Locate and identify every blood parasite.
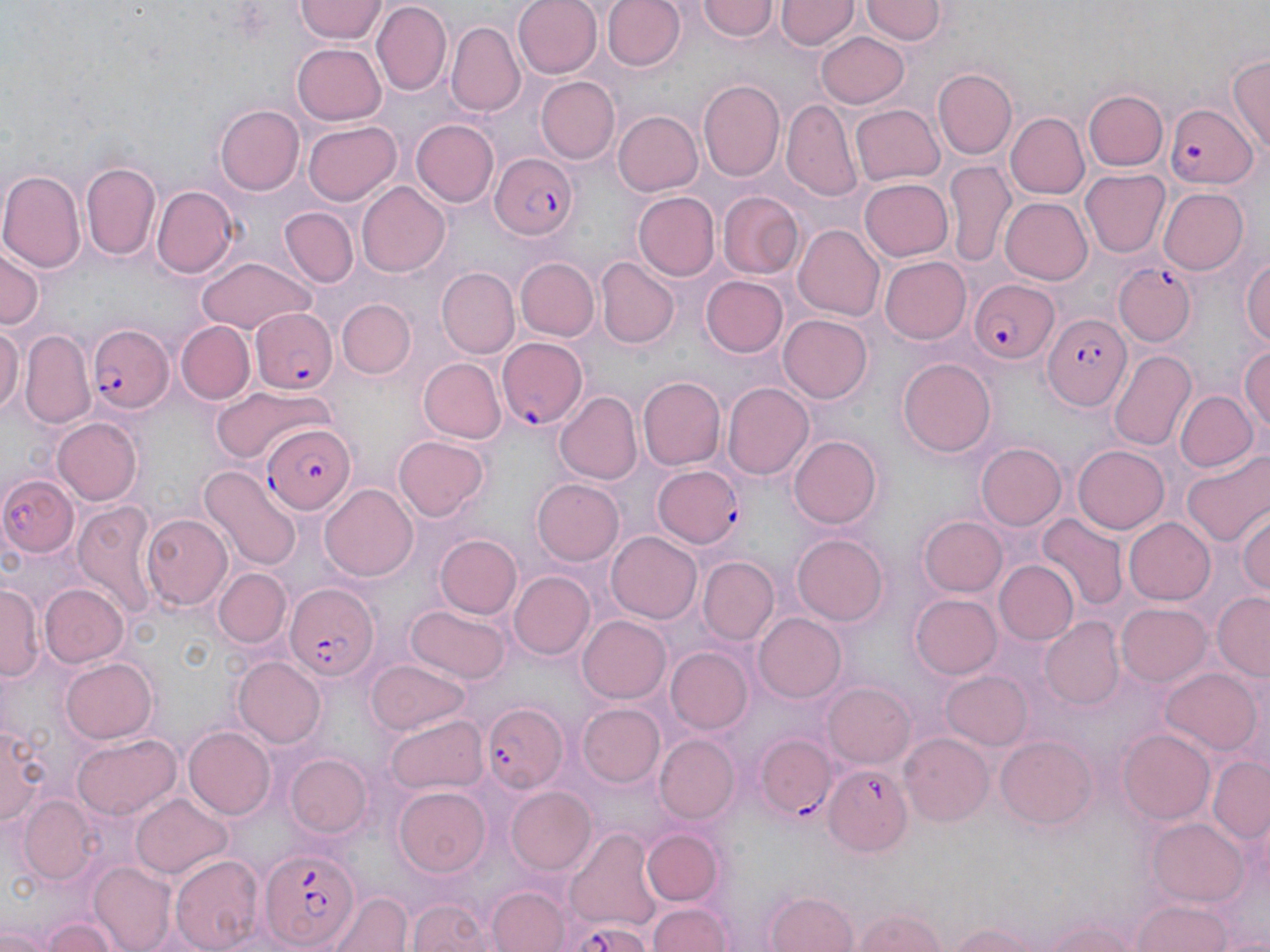

Approximate bounding boxes as (x1,y1)-(x2,y2) corner pairs in pixels.
Plasmodium falciparum-infected red blood cells: (1167,101)-(1258,192), (487,152)-(578,242), (1117,265)-(1196,346), (967,279)-(1058,365), (250,309)-(337,393), (1040,312)-(1132,412), (88,322)-(175,414), (498,337)-(588,430), (263,424)-(354,512), (652,464)-(742,548), (284,585)-(380,678), (479,701)-(567,793), (757,736)-(836,816), (821,764)-(910,856), (260,847)-(358,952).
No Plasmodium ovale, Plasmodium malariae, Plasmodium vivax, Babesia divergens, or Trypanosoma brucei observed.

Uninfected red blood cell locations: (295,0)-(386,42), (513,0)-(602,79), (602,0)-(684,72), (372,1)-(453,94), (778,1)-(857,50), (697,2)-(779,44), (861,2)-(945,46), (447,21)-(525,115), (816,32)-(911,108), (293,40)-(388,124), (1230,54)-(1270,154), (932,68)-(1017,160), (535,76)-(620,164), (698,80)-(784,180), (1085,90)-(1167,171), (782,101)-(861,199), (851,103)-(945,186), (215,105)-(304,195), (612,111)-(702,197), (1006,113)-(1090,199), (304,119)-(400,204), (413,121)-(497,207), (945,159)-(1013,265), (81,160)-(161,261), (0,168)-(85,273), (1080,168)-(1172,257), (859,177)-(953,263), (356,182)-(451,278), (153,185)-(237,278), (1157,187)-(1249,276), (717,189)-(804,278), (631,192)-(719,281), (1001,198)-(1091,285), (282,208)-(358,288), (793,223)-(884,321), (0,242)-(43,333), (1241,252)-(1270,347), (880,256)-(971,345), (518,258)-(599,341), (196,259)-(317,335), (596,260)-(678,349), (438,269)-(520,357), (701,275)-(789,358), (337,297)-(416,378), (778,314)-(872,404), (0,320)-(21,415), (176,320)-(254,402), (22,332)-(95,429), (1240,345)-(1270,437), (1108,347)-(1196,453), (420,358)-(506,445), (898,358)-(996,457), (639,376)-(726,470), (722,383)-(812,480), (213,385)-(337,460), (1175,390)-(1256,472), (553,391)-(641,485), (53,417)-(143,504), (393,434)-(489,522), (788,435)-(883,529), (976,443)-(1068,532), (1072,446)-(1168,534), (1186,449)-(1270,548), (201,466)-(299,571), (0,474)-(80,558), (532,477)-(623,563), (322,485)-(417,581), (72,499)-(157,620), (1236,507)-(1270,600), (142,513)-(232,609), (1040,515)-(1124,609), (918,516)-(1005,597), (1123,516)-(1216,604), (607,531)-(702,625), (793,533)-(890,625), (438,534)-(521,618), (698,557)-(779,644), (995,561)-(1079,645), (213,568)-(289,647), (509,572)-(593,660), (40,583)-(129,668), (1,584)-(40,682), (1212,593)-(1270,677), (912,594)-(1001,678), (408,604)-(508,682), (1117,604)-(1213,687), (754,614)-(846,703), (578,615)-(671,703), (1041,618)-(1126,708), (666,648)-(752,734), (232,656)-(326,747), (59,657)-(158,744), (369,659)-(469,735), (1163,668)-(1263,757), (941,671)-(1034,751), (823,684)-(915,768), (580,704)-(666,787), (387,714)-(487,794), (3,715)-(51,830), (184,727)-(275,820), (1118,730)-(1216,824), (74,733)-(178,817), (901,733)-(993,824), (656,736)-(737,823), (995,737)-(1096,827), (285,754)-(369,837), (1209,756)-(1270,845), (395,786)-(492,875), (505,786)-(596,874), (133,795)-(234,880), (20,797)-(97,882), (1148,816)-(1251,909), (641,829)-(721,905), (566,832)-(662,931), (171,855)-(262,951), (92,860)-(176,950), (490,887)-(569,952), (331,889)-(411,952), (768,893)-(857,952), (409,897)-(495,952), (1132,901)-(1237,952), (647,902)-(732,952), (850,908)-(951,952), (38,916)-(124,952), (1036,916)-(1146,952), (942,919)-(1062,952). Slide-level diagnosis: Plasmodium falciparum. Light microscopy. Captured at 1000x magnification. Single field of view. May-Grünwald-Giemsa-stained preparation. Thin blood smear. Image is 1270×952 pixels.